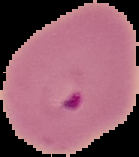

malaria status = parasitized
preparation = thin blood film
image type = cell region segmented out of the field of view; surrounding area masked to black
image size = 139×157 pixels